Locate every blood parasite and identify its species.
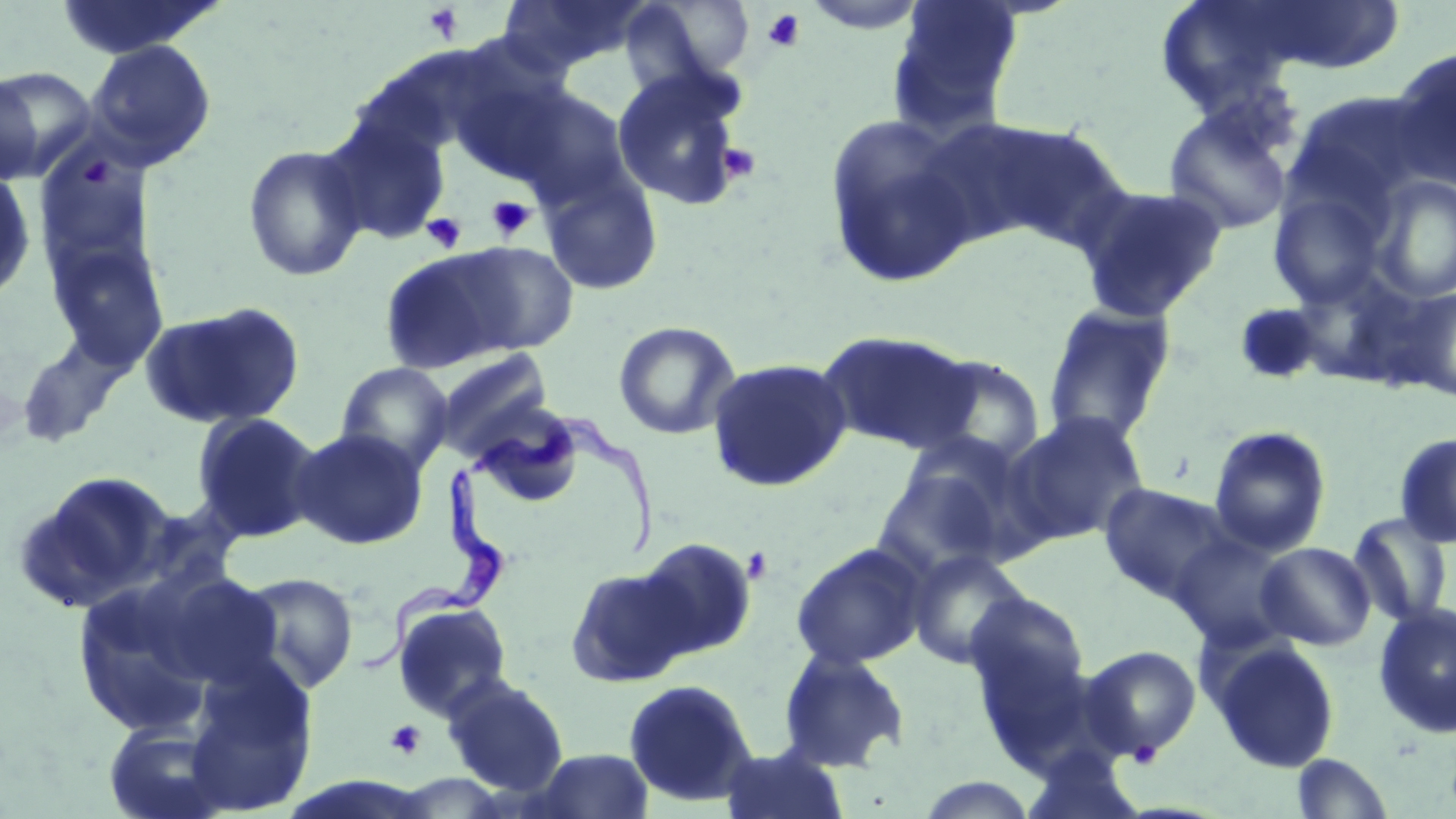

Approximate bounding boxes as (x1, y1, x2, y2) in pixels.
Trypanosoma brucei: (468, 416, 659, 554), (361, 462, 502, 673).
No Plasmodium falciparum, Plasmodium ovale, Plasmodium malariae, Plasmodium vivax, or Babesia divergens observed.

Platelet locations: (423, 3, 464, 43), (762, 8, 805, 52), (717, 141, 760, 183), (486, 195, 535, 241), (422, 213, 466, 252), (745, 551, 771, 582), (385, 719, 425, 759), (1127, 740, 1163, 768). Uninfected red blood cell locations: (50, 0, 226, 60), (497, 0, 650, 74), (620, 0, 756, 92), (887, 0, 1024, 136), (1155, 0, 1308, 116), (1240, 1, 1408, 76), (85, 39, 216, 170), (1388, 48, 1456, 190), (0, 66, 98, 181), (612, 68, 747, 210), (0, 71, 44, 185), (511, 88, 634, 206), (1283, 88, 1430, 224), (1163, 105, 1294, 236), (322, 114, 452, 244), (823, 114, 982, 290), (963, 120, 1133, 252), (242, 143, 369, 283), (539, 166, 664, 294), (0, 168, 38, 302), (1370, 174, 1456, 303), (1074, 182, 1228, 323), (1267, 184, 1394, 312), (447, 240, 579, 356), (46, 241, 170, 370), (377, 248, 521, 373), (1389, 287, 1456, 403), (140, 301, 305, 431), (1233, 303, 1325, 386), (1042, 304, 1177, 446), (612, 321, 740, 440), (816, 330, 980, 454), (15, 334, 134, 448), (431, 348, 554, 459), (906, 353, 1046, 470), (706, 357, 853, 492), (335, 362, 454, 475), (470, 400, 585, 505), (190, 411, 325, 543), (1004, 411, 1150, 547), (1208, 425, 1331, 556), (291, 426, 429, 550), (1394, 431, 1456, 549), (871, 462, 1016, 583), (21, 470, 180, 610), (1097, 482, 1237, 604), (136, 499, 245, 593), (1347, 512, 1454, 628), (1169, 531, 1297, 653), (632, 537, 759, 661), (1254, 541, 1376, 652), (790, 542, 929, 670), (907, 550, 1030, 670), (564, 562, 695, 688), (143, 568, 288, 691), (70, 571, 235, 737), (235, 572, 359, 694), (964, 591, 1089, 716), (391, 600, 513, 721), (1373, 602, 1456, 738), (1208, 639, 1342, 773), (1080, 645, 1202, 761), (776, 648, 909, 771), (181, 659, 320, 816), (441, 675, 570, 796), (623, 678, 758, 807), (103, 720, 231, 819), (719, 745, 851, 818), (531, 748, 653, 819), (1290, 753, 1394, 818). Slide-level diagnosis: Trypanosoma brucei. May-Grünwald-Giemsa-stained preparation. Image is 1456×819 pixels. One field of a larger specimen. Light microscopy. Captured at 1000x magnification. Thin blood film.